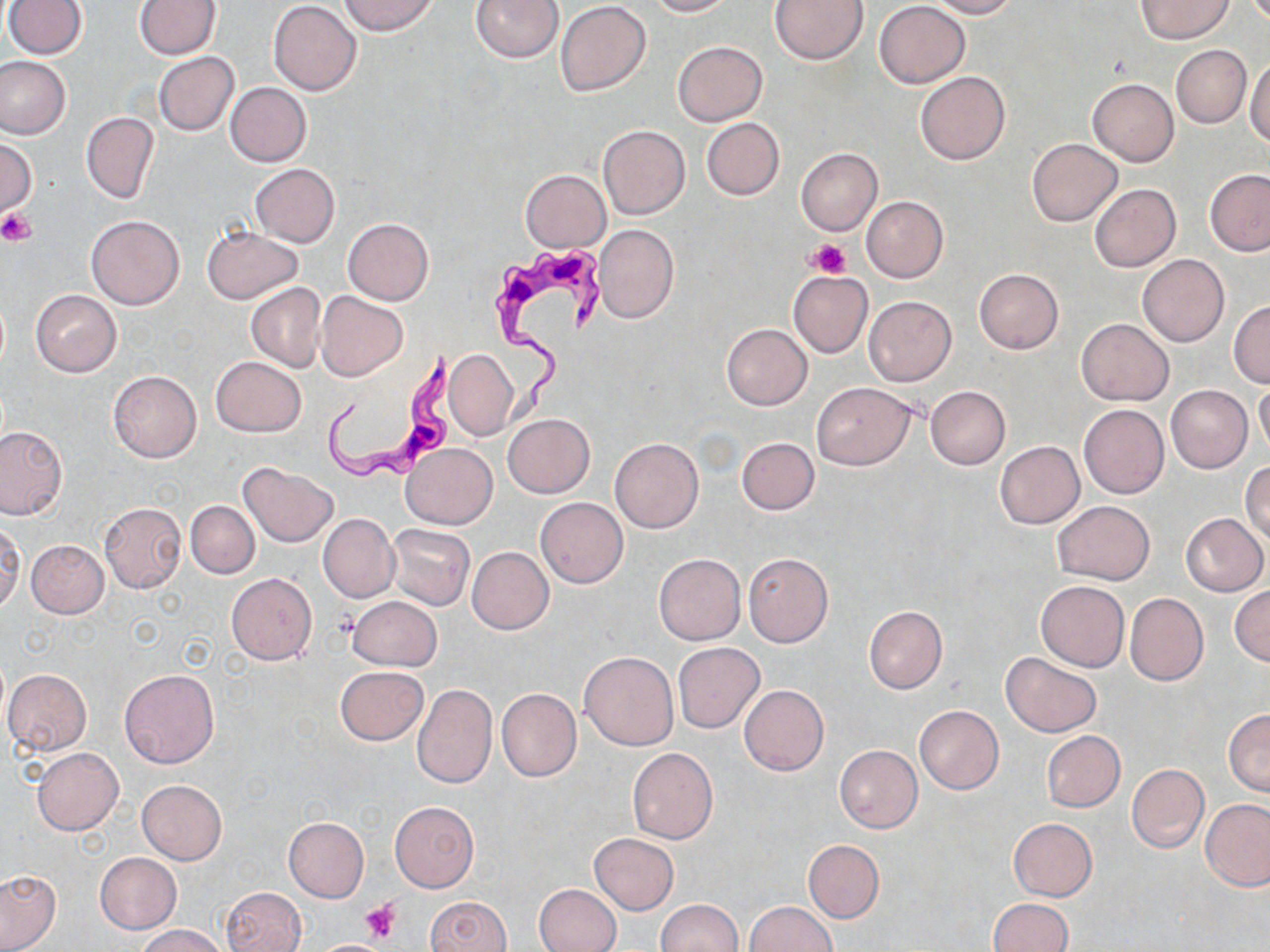

Summary:
  - Coordinate format: approximate bounding boxes as (x1,y1)-(x2,y2) corner pairs in pixels
  - Platelet locations: (0,208)-(37,246), (809,239)-(850,279), (360,898)-(402,946)
  - Trypanosoma brucei locations: (492,239)-(604,419), (321,348)-(456,487)
  - Uninfected red blood cell locations: (4,0)-(86,59), (339,0)-(438,35), (472,0)-(564,63), (644,0)-(734,16), (770,0)-(867,65), (928,0)-(1019,18), (1135,0)-(1233,43), (134,1)-(220,59), (269,1)-(361,95), (555,2)-(651,96), (875,2)-(970,87), (673,41)-(767,126), (1171,45)-(1251,127), (154,53)-(238,135), (0,56)-(71,139), (1245,59)-(1270,148), (915,71)-(1010,165), (1087,79)-(1178,166), (226,83)-(311,166), (81,112)-(159,204), (701,118)-(784,200), (598,125)-(690,219), (1028,138)-(1121,226), (0,139)-(37,219), (796,147)-(883,236), (249,163)-(339,247), (521,169)-(610,253), (1204,169)-(1270,256), (1090,183)-(1181,272), (862,196)-(948,282), (86,214)-(184,310), (342,217)-(434,305), (594,224)-(678,323), (202,228)-(303,304), (1137,254)-(1230,346), (974,269)-(1064,354), (788,271)-(873,356), (246,283)-(327,372), (30,290)-(122,376), (315,291)-(407,381), (864,296)-(956,386), (1229,301)-(1270,387), (1077,319)-(1174,406), (722,323)-(812,409), (443,347)-(518,441), (211,357)-(304,437), (108,371)-(201,463), (1254,382)-(1270,458), (810,383)-(917,469), (925,385)-(1011,469), (1167,386)-(1252,472), (1079,404)-(1169,499), (503,414)-(595,497), (0,426)-(66,519), (610,437)-(703,533), (737,437)-(819,514), (994,441)-(1085,529), (403,444)-(497,530), (1241,462)-(1270,547), (240,464)-(338,546), (536,497)-(627,588), (185,500)-(258,578), (1052,501)-(1155,583), (99,502)-(187,593), (1182,513)-(1268,596), (318,514)-(398,603), (0,521)-(23,612), (388,523)-(475,611), (26,539)-(108,617), (467,547)-(553,635), (742,552)-(833,647), (654,554)-(746,644), (226,573)-(317,665), (1035,581)-(1130,672), (1229,586)-(1269,666), (1125,593)-(1208,686), (348,596)-(441,670), (864,605)-(948,693), (673,642)-(764,732), (579,652)-(679,751), (1001,653)-(1102,737), (336,665)-(428,745), (118,668)-(218,768), (3,669)-(91,754), (413,684)-(497,788), (739,684)-(828,775), (496,687)-(581,782), (915,705)-(1003,794), (1224,709)-(1270,796), (1041,730)-(1125,812), (834,745)-(922,833), (31,748)-(123,835), (627,748)-(717,844), (1127,764)-(1209,852), (136,779)-(227,864), (1200,798)-(1270,891), (390,800)-(479,892), (284,817)-(368,901), (1008,818)-(1097,902), (590,833)-(678,914), (803,841)-(884,922), (95,852)-(181,933), (0,870)-(60,950), (533,883)-(621,952), (222,886)-(306,952), (424,896)-(512,952), (986,898)-(1072,952), (658,899)-(743,952), (743,902)-(836,952), (137,924)-(230,952)
  - Slide-level diagnosis: Trypanosoma brucei
  - Field of view: one of a larger specimen
  - Stain: May-Grünwald-Giemsa
  - Preparation: thin blood smear
  - Image size: 1270×952 pixels
  - Modality: optical microscopy
  - Magnification: 1000x